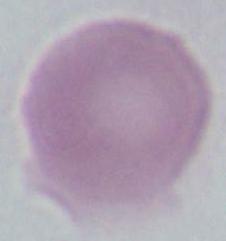

{
  "identification": "red blood cell",
  "magnification": "1000x",
  "modality": "micrograph"
}